Identify the blood parasite species.
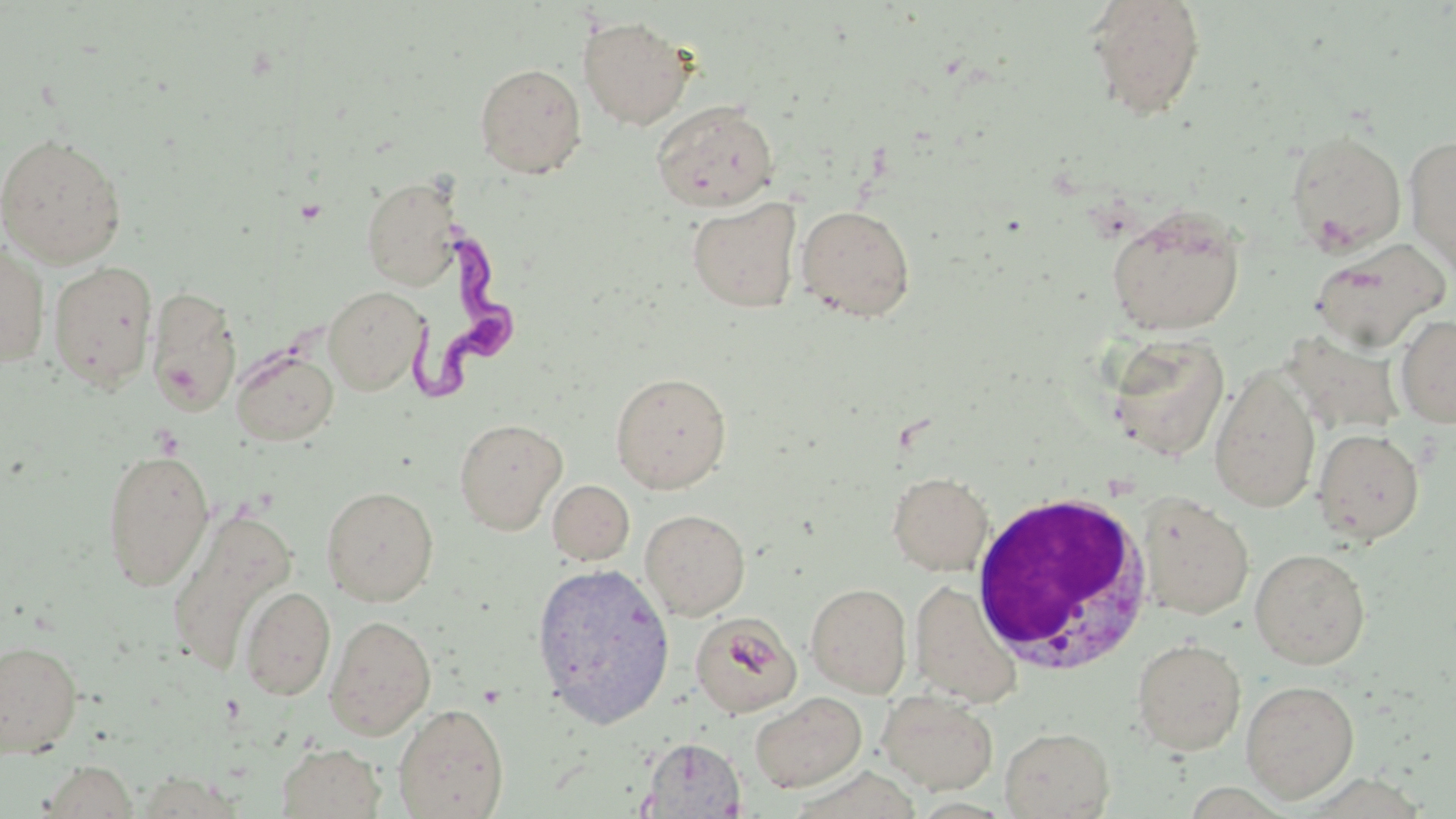

Trypanosoma brucei.

uninfected red blood cell locations = approximate bounding boxes as (x1,y1)-(x2,y2) corner pairs in pixels: (1085,0)-(1207,121), (578,16)-(693,130), (474,63)-(587,178), (651,100)-(780,212), (1284,128)-(1407,255), (0,132)-(127,267), (1403,134)-(1456,273), (360,176)-(462,291), (687,198)-(802,313), (796,204)-(916,321), (1105,204)-(1246,336), (1309,238)-(1449,352), (0,239)-(51,368), (48,260)-(158,391), (145,285)-(242,417), (323,286)-(428,395), (1395,314)-(1456,427), (1106,332)-(1230,463), (232,347)-(338,446), (1209,365)-(1322,513), (610,371)-(732,493), (453,417)-(568,534), (1312,427)-(1425,544), (101,448)-(214,591), (887,471)-(994,575), (547,479)-(635,565), (321,485)-(439,606), (1136,492)-(1254,620), (166,508)-(296,676), (640,509)-(750,620), (1250,548)-(1371,669), (531,561)-(675,725), (909,580)-(1022,707), (806,582)-(912,697), (239,586)-(335,701), (690,612)-(801,717), (325,614)-(436,739), (1131,637)-(1247,755), (0,639)-(83,757), (1240,679)-(1360,802), (878,690)-(999,795), (749,692)-(866,793), (393,703)-(509,818), (1000,726)-(1114,819), (641,737)-(746,818), (276,742)-(385,818), (35,761)-(137,817), (134,771)-(249,817)
image size = 1456×819 pixels
stain = May-Grünwald-Giemsa
modality = light microscopy
magnification = 1000x
preparation = thin blood smear
field of view = one of a larger specimen
Trypanosoma brucei locations = approximate bounding boxes as (x1,y1)-(x2,y2) corner pairs in pixels: (385,218)-(509,414)
white blood cell locations = approximate bounding boxes as (x1,y1)-(x2,y2) corner pairs in pixels: (969,488)-(1155,676)